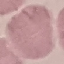
Result: no malaria parasites seen. Thin blood smear. Cell patch, automatically extracted from a larger field of view and resized to 64 × 64 pixels. Photographed with a smartphone camera at the microscope eyepiece. Giemsa stain.